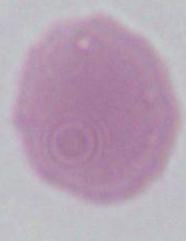
1000x magnification. A red blood cell is seen. Photomicrograph.